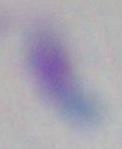
Summary:
  - Magnification: 1000x
  - Modality: photomicrograph
  - Identification: Toxoplasma gondii